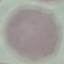 Malaria status: uninfected. Thin blood smear. Automatically extracted cell patch, resized to 64 × 64 pixels. Giemsa stain. Photographed with a smartphone camera at the microscope eyepiece.